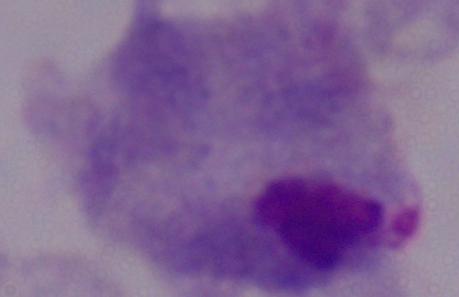

Summary:
  - Identification: trichomonad
  - Modality: photomicrograph
  - Magnification: 1000x